Assess this cell for malaria.
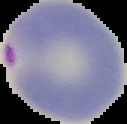

Parasitized.

preparation = thin blood smear
image type = cell region segmented out of the field of view; surrounding area masked to black
image size = 127×124 pixels